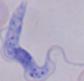

Micrograph. A trypanosome is shown. Captured at 1000x magnification.